Assess this cell for malaria.
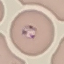

Parasitized.

{
  "stain": "Giemsa",
  "preparation": "thin blood film",
  "capture": "smartphone through the microscope eyepiece",
  "image_type": "automatically extracted cell patch, resized to 64 × 64 pixels"
}